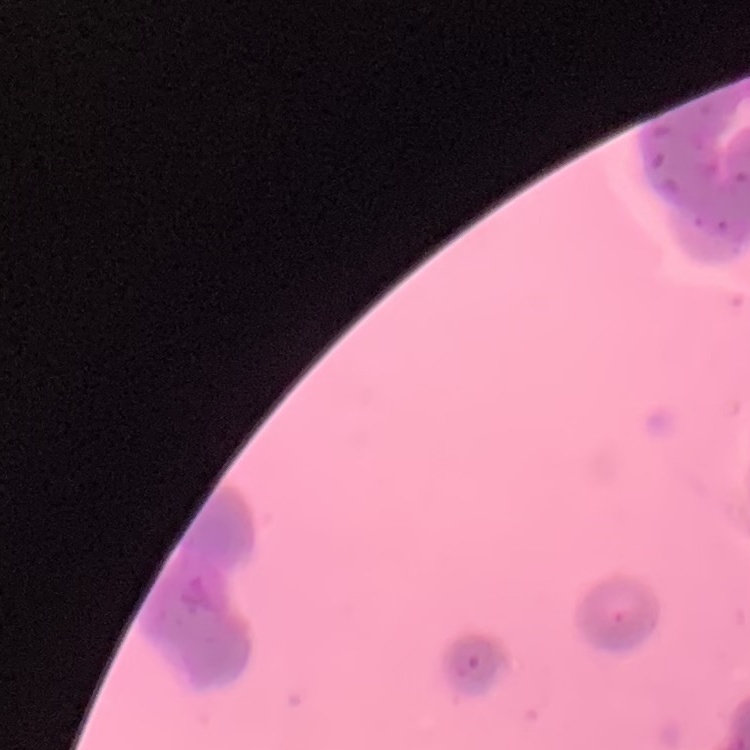

Summary:
  - Erythrocyte morphology: rouleaux formation
  - Stain: Field's or Giemsa
  - Preparation: thin peripheral smear
  - Image type: one tile cut from a larger photomicrograph